Assess the morphology of the erythrocytes.
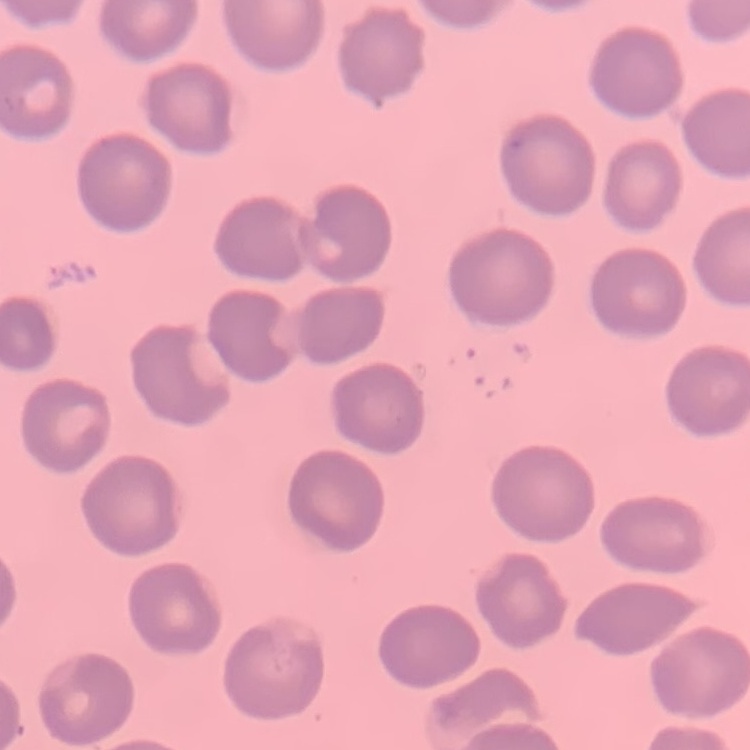

No rouleaux formation.

Summary:
  - Stain: Field's or Giemsa
  - Preparation: thin blood smear
  - Image type: square crop of a larger photomicrograph